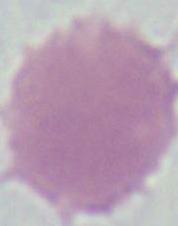
Summary:
  - Modality: micrograph
  - Magnification: 1000x
  - Identification: erythrocyte